Name the parasite shown.
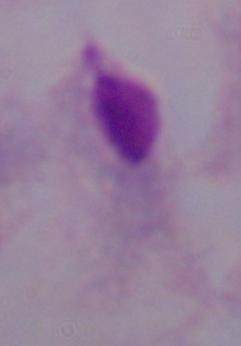

This is a trichomonad.

Summary:
  - Modality: micrograph
  - Magnification: 1000x